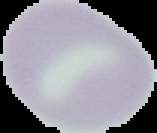

Summary:
  - Image type: segmented cell region on a black background
  - Result: no malaria parasites seen
  - Preparation: thin blood smear
  - Image size: 157×133 pixels